State the blood parasite species.
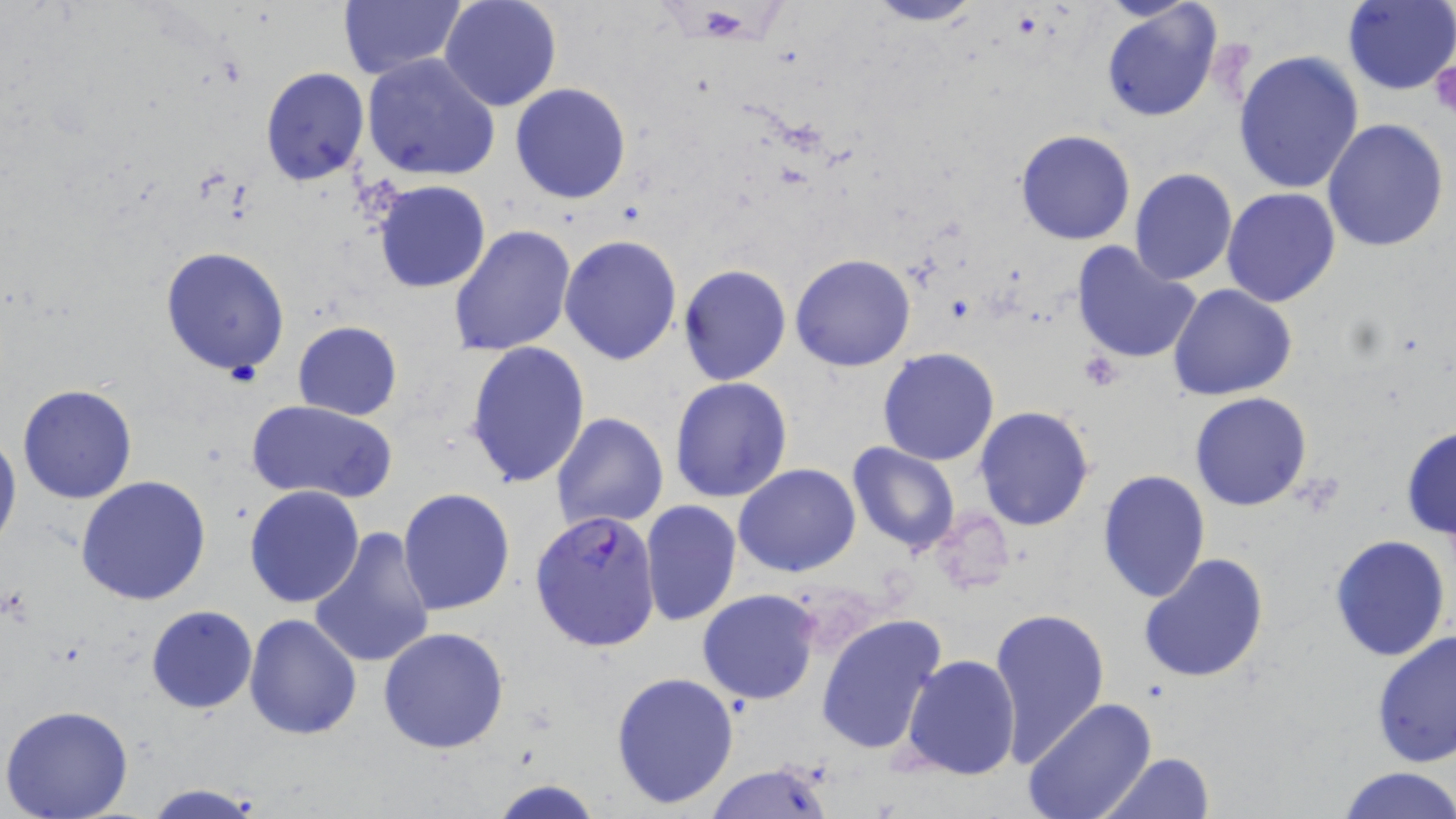
Plasmodium falciparum.

Approximate bounding boxes as named x1/y1/x2/y2 corners in pixels. Uninfected red blood cell locations: (x1=439, y1=0, x2=562, y2=112), (x1=857, y1=0, x2=987, y2=27), (x1=1343, y1=0, x2=1456, y2=95), (x1=338, y1=1, x2=466, y2=80), (x1=1099, y1=4, x2=1222, y2=124), (x1=467, y1=34, x2=604, y2=181), (x1=1234, y1=51, x2=1365, y2=196), (x1=361, y1=53, x2=501, y2=182), (x1=260, y1=66, x2=369, y2=186), (x1=510, y1=82, x2=631, y2=205), (x1=1322, y1=118, x2=1451, y2=253), (x1=1014, y1=129, x2=1138, y2=246), (x1=1128, y1=168, x2=1237, y2=286), (x1=374, y1=180, x2=490, y2=293), (x1=1222, y1=188, x2=1341, y2=308), (x1=449, y1=224, x2=577, y2=356), (x1=558, y1=234, x2=682, y2=366), (x1=1071, y1=239, x2=1204, y2=366), (x1=160, y1=245, x2=292, y2=379), (x1=790, y1=254, x2=915, y2=372), (x1=678, y1=265, x2=791, y2=386), (x1=1168, y1=283, x2=1298, y2=402), (x1=292, y1=321, x2=402, y2=421), (x1=464, y1=342, x2=591, y2=489), (x1=878, y1=347, x2=999, y2=465), (x1=669, y1=376, x2=794, y2=503), (x1=16, y1=384, x2=138, y2=505), (x1=1189, y1=391, x2=1312, y2=510), (x1=246, y1=398, x2=397, y2=503), (x1=975, y1=406, x2=1093, y2=531), (x1=551, y1=412, x2=668, y2=531), (x1=0, y1=426, x2=21, y2=556), (x1=1400, y1=426, x2=1456, y2=544), (x1=847, y1=441, x2=960, y2=553), (x1=734, y1=464, x2=860, y2=578), (x1=1098, y1=470, x2=1211, y2=602), (x1=76, y1=475, x2=212, y2=606), (x1=244, y1=484, x2=364, y2=608), (x1=397, y1=490, x2=515, y2=615), (x1=639, y1=501, x2=741, y2=627), (x1=930, y1=508, x2=1013, y2=596), (x1=310, y1=528, x2=436, y2=669), (x1=1328, y1=533, x2=1452, y2=661), (x1=1138, y1=552, x2=1270, y2=684), (x1=697, y1=589, x2=821, y2=705), (x1=145, y1=605, x2=258, y2=714), (x1=988, y1=606, x2=1110, y2=768), (x1=816, y1=613, x2=949, y2=759), (x1=243, y1=614, x2=362, y2=738), (x1=378, y1=627, x2=510, y2=753), (x1=1372, y1=628, x2=1456, y2=770), (x1=902, y1=653, x2=1021, y2=780), (x1=610, y1=670, x2=740, y2=809), (x1=1022, y1=697, x2=1156, y2=819), (x1=1, y1=703, x2=134, y2=819), (x1=1098, y1=752, x2=1216, y2=818), (x1=703, y1=762, x2=834, y2=819), (x1=1333, y1=765, x2=1456, y2=819), (x1=487, y1=778, x2=606, y2=819), (x1=144, y1=784, x2=265, y2=818). Plasmodium falciparum-infected red blood cell locations: (x1=531, y1=508, x2=661, y2=653). Platelet locations: (x1=1431, y1=57, x2=1456, y2=114), (x1=1078, y1=352, x2=1123, y2=390). Image is 1456×819 pixels. May-Grünwald-Giemsa-stained preparation. Optical microscopy. Thin blood film. 1000x magnification. One field of a larger specimen.